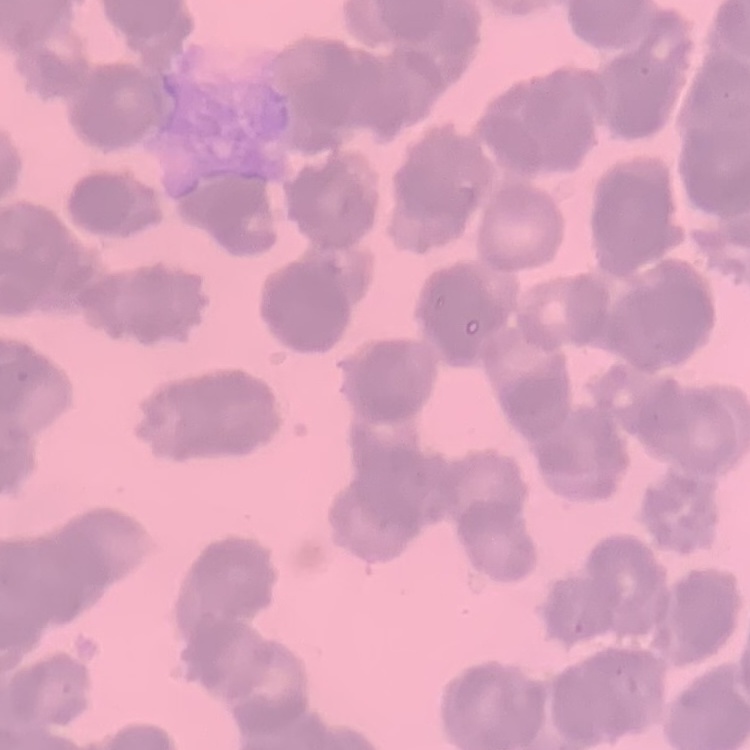
red blood cell morphology = rouleaux formation
preparation = thin peripheral smear
stain = Field's or Giemsa
image type = one tile cut from a larger photomicrograph